Describe the morphology of the erythrocytes.
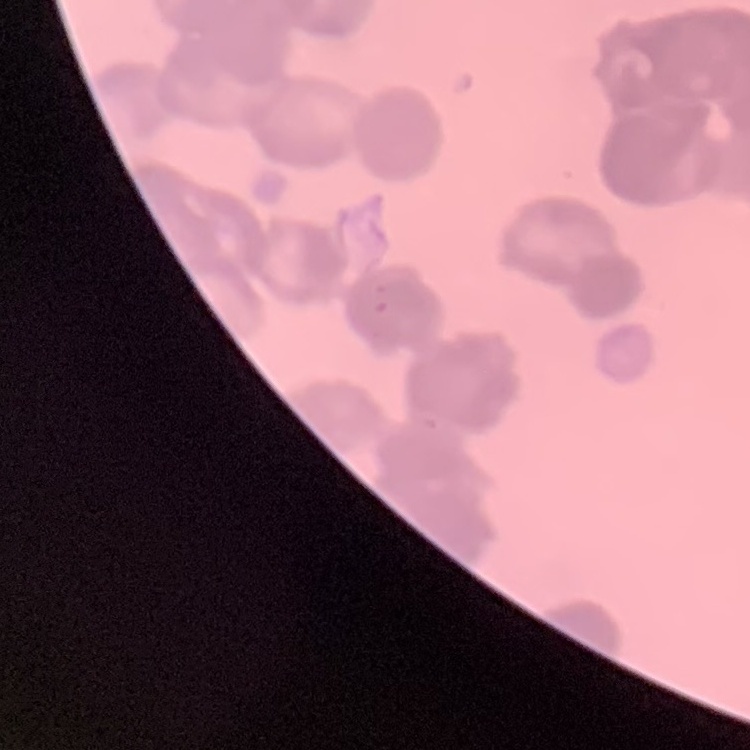

They show rouleaux formation.

One tile cut from a larger photomicrograph. Thin blood smear. Field's or Giemsa stain.